Assess this cell for malaria.
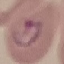
It is parasitized.

preparation: thin blood smear
stain: Giemsa
capture: smartphone camera at the microscope eyepiece
image_type: automatically extracted cell patch, resized to 64 × 64 pixels